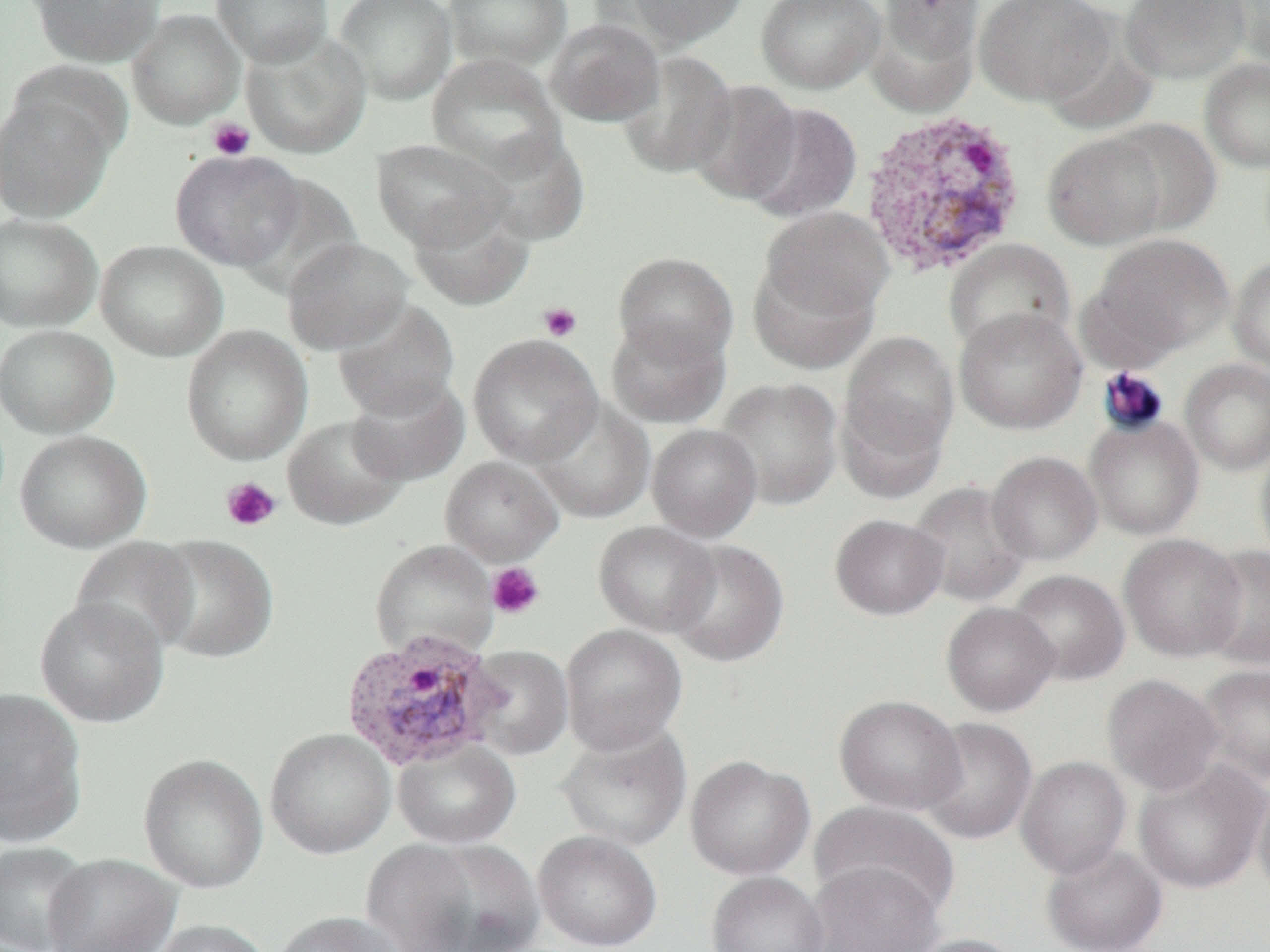
Summary:
  - Coordinate format: approximate bounding boxes as named x1/y1/x2/y2 corners in pixels
  - Platelet locations (subset): (x1=207, y1=118, x2=255, y2=161), (x1=538, y1=302, x2=582, y2=342), (x1=221, y1=477, x2=281, y2=532), (x1=486, y1=562, x2=546, y2=620)
  - Uninfected red blood cell locations (subset): (x1=29, y1=0, x2=164, y2=67), (x1=212, y1=0, x2=334, y2=66), (x1=334, y1=0, x2=458, y2=105), (x1=443, y1=0, x2=572, y2=72), (x1=607, y1=0, x2=753, y2=49), (x1=756, y1=0, x2=885, y2=94), (x1=868, y1=0, x2=982, y2=109), (x1=974, y1=0, x2=1115, y2=106), (x1=1120, y1=0, x2=1250, y2=84), (x1=1220, y1=0, x2=1270, y2=72), (x1=127, y1=9, x2=245, y2=129), (x1=545, y1=18, x2=665, y2=126), (x1=241, y1=29, x2=372, y2=158), (x1=617, y1=50, x2=737, y2=178), (x1=426, y1=54, x2=566, y2=176), (x1=1199, y1=58, x2=1270, y2=173), (x1=688, y1=80, x2=802, y2=205), (x1=0, y1=89, x2=118, y2=223), (x1=741, y1=102, x2=863, y2=223), (x1=1107, y1=118, x2=1223, y2=235), (x1=472, y1=130, x2=591, y2=245), (x1=1041, y1=130, x2=1168, y2=250), (x1=371, y1=139, x2=511, y2=251), (x1=170, y1=149, x2=307, y2=271), (x1=407, y1=196, x2=534, y2=310), (x1=759, y1=207, x2=894, y2=322), (x1=0, y1=213, x2=102, y2=332), (x1=1083, y1=234, x2=1235, y2=364), (x1=282, y1=236, x2=413, y2=355), (x1=943, y1=238, x2=1075, y2=356), (x1=95, y1=240, x2=228, y2=362), (x1=613, y1=251, x2=739, y2=366), (x1=1228, y1=256, x2=1270, y2=374), (x1=748, y1=258, x2=879, y2=374), (x1=332, y1=299, x2=460, y2=420), (x1=954, y1=307, x2=1087, y2=434), (x1=606, y1=317, x2=731, y2=429), (x1=0, y1=324, x2=119, y2=438), (x1=181, y1=325, x2=313, y2=466), (x1=837, y1=329, x2=959, y2=480), (x1=468, y1=333, x2=603, y2=467), (x1=1179, y1=358, x2=1270, y2=475), (x1=346, y1=375, x2=470, y2=486), (x1=714, y1=377, x2=843, y2=510), (x1=532, y1=397, x2=655, y2=523), (x1=1084, y1=414, x2=1204, y2=540), (x1=282, y1=415, x2=410, y2=530), (x1=647, y1=424, x2=762, y2=541), (x1=14, y1=430, x2=151, y2=553), (x1=1254, y1=436, x2=1270, y2=571), (x1=986, y1=451, x2=1103, y2=566), (x1=907, y1=481, x2=1031, y2=607), (x1=830, y1=513, x2=948, y2=620), (x1=593, y1=521, x2=720, y2=637), (x1=1119, y1=534, x2=1247, y2=661), (x1=146, y1=535, x2=279, y2=664), (x1=70, y1=537, x2=200, y2=655), (x1=666, y1=539, x2=790, y2=667), (x1=1200, y1=545, x2=1270, y2=671), (x1=1006, y1=569, x2=1130, y2=685), (x1=34, y1=596, x2=169, y2=728), (x1=940, y1=602, x2=1060, y2=716), (x1=560, y1=623, x2=687, y2=755), (x1=465, y1=645, x2=573, y2=759), (x1=1195, y1=664, x2=1270, y2=787), (x1=1102, y1=674, x2=1224, y2=795), (x1=0, y1=686, x2=88, y2=847), (x1=835, y1=695, x2=966, y2=814), (x1=917, y1=717, x2=1037, y2=845), (x1=555, y1=723, x2=692, y2=852), (x1=265, y1=727, x2=396, y2=859), (x1=392, y1=739, x2=521, y2=848), (x1=137, y1=752, x2=268, y2=894), (x1=684, y1=755, x2=814, y2=880), (x1=1016, y1=755, x2=1131, y2=878), (x1=1132, y1=759, x2=1270, y2=894), (x1=1253, y1=777, x2=1270, y2=901), (x1=809, y1=802, x2=960, y2=919), (x1=533, y1=830, x2=663, y2=951), (x1=412, y1=838, x2=545, y2=952), (x1=360, y1=839, x2=483, y2=952), (x1=0, y1=841, x2=93, y2=952), (x1=1041, y1=843, x2=1168, y2=951), (x1=42, y1=853, x2=181, y2=952), (x1=805, y1=862, x2=944, y2=952), (x1=706, y1=871, x2=829, y2=952), (x1=273, y1=911, x2=408, y2=952), (x1=149, y1=919, x2=274, y2=952), (x1=903, y1=934, x2=1027, y2=952)
  - Plasmodium vivax-infected red blood cell locations: (x1=859, y1=108, x2=1028, y2=278), (x1=339, y1=629, x2=506, y2=772)
  - Slide-level diagnosis: Plasmodium vivax
  - Image size: 1270×952 pixels
  - Magnification: 1000x
  - Field of view: one of a larger specimen
  - Modality: optical microscopy
  - Preparation: thin blood smear